Comment on the morphology of the red blood cells.
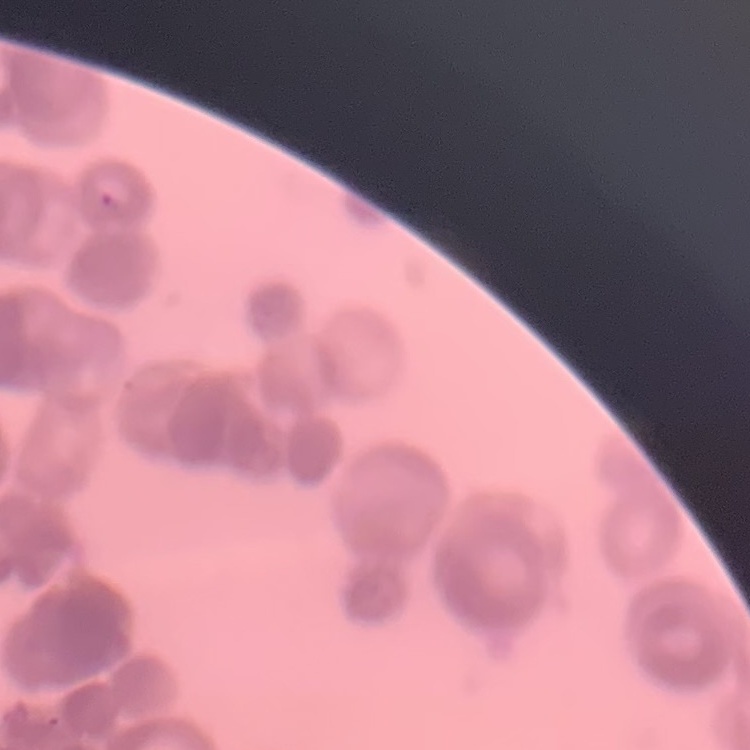
Rouleaux formation.

image type = square crop of a larger photomicrograph
stain = Field's or Giemsa
preparation = thin blood smear